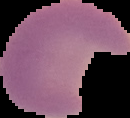 Image is 130×118 pixels. The area outside the segmented cell region is set to black. From a thin blood smear. Malaria status: parasitized.